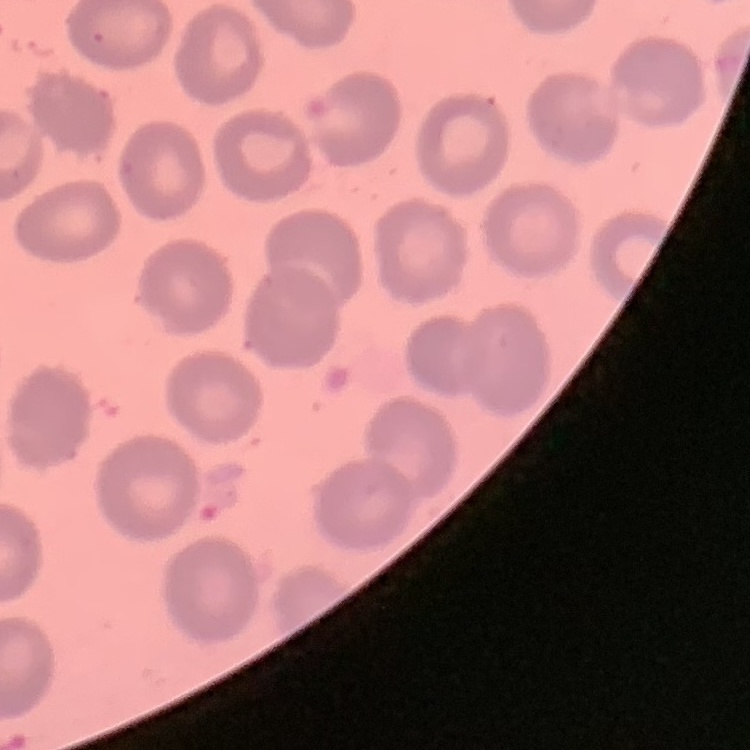

The erythrocytes exhibit no rouleaux formation. One tile cut from a larger photomicrograph. Stained with either Field's or Giemsa. Thin blood smear.